Describe the morphology of the red blood cells.
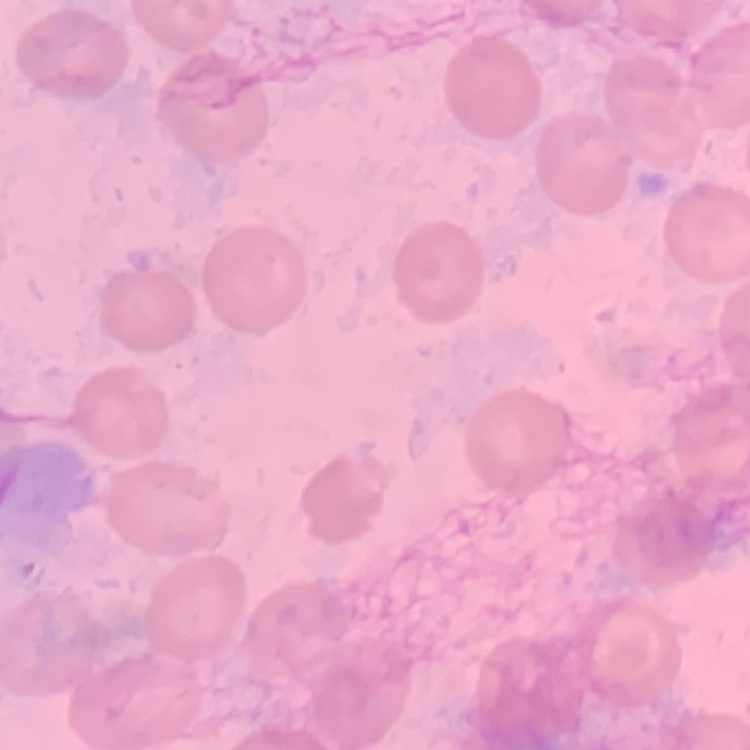

They show no rouleaux formation.

Thin blood smear. Square crop of a larger photomicrograph. Stained with either Field's or Giemsa.